Describe the morphology of the red blood cells.
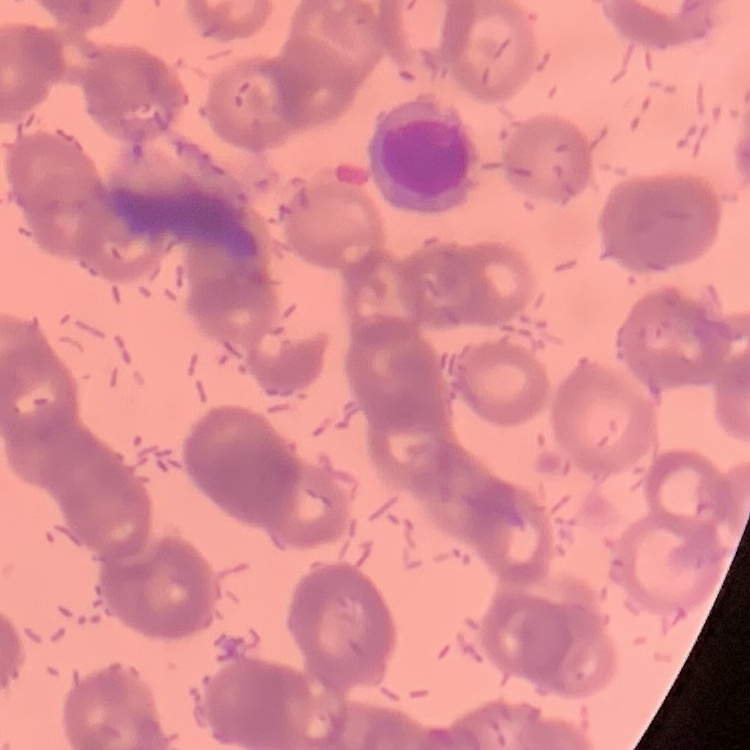
Rouleaux formation.

Stained with either Field's or Giemsa. One tile cut from a larger photomicrograph. Thin peripheral smear.